Mark where platelets are.
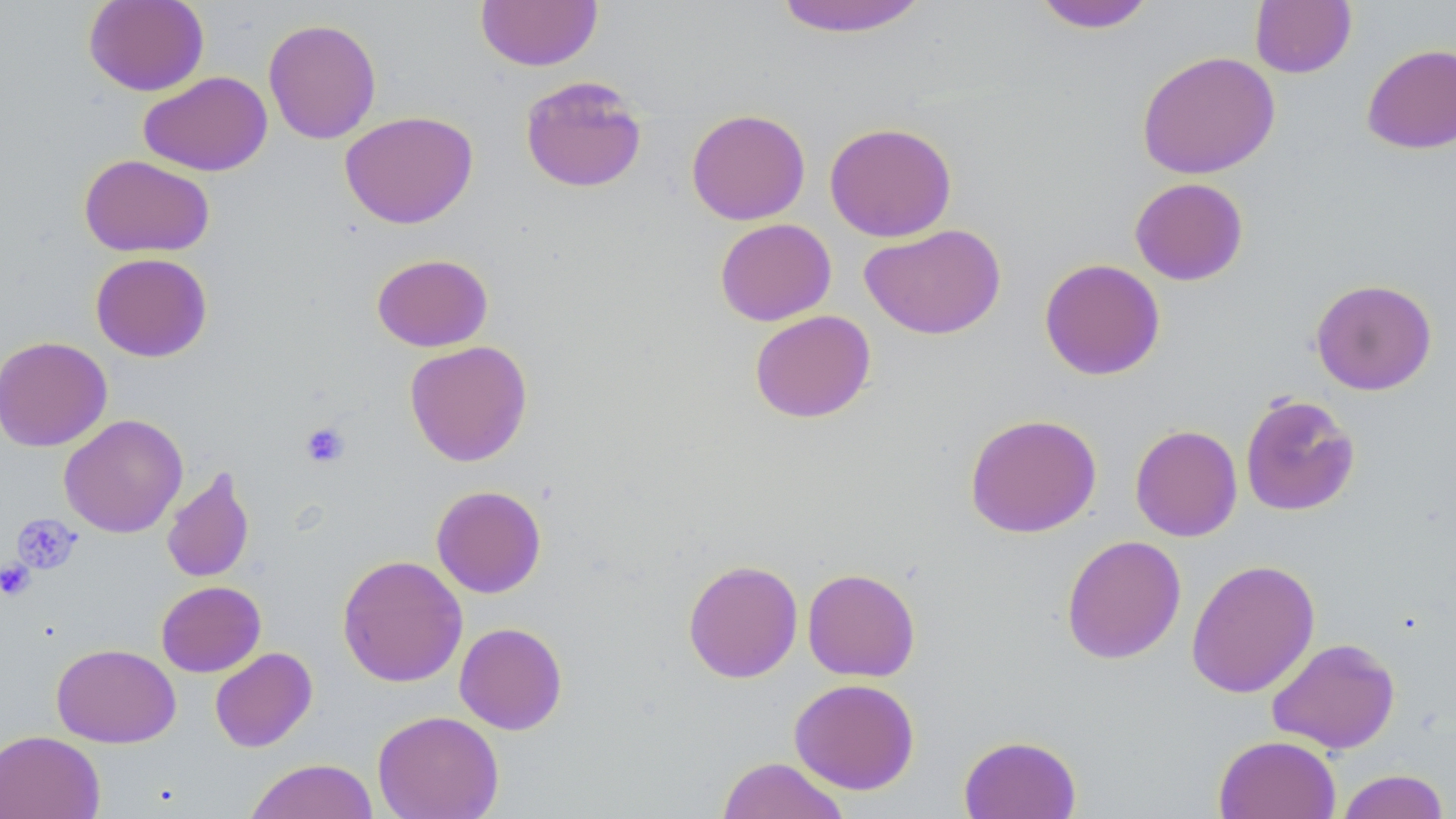

Approximate bounding boxes as [x1, y1, x2, y2] in pixels.
Platelets: [300, 421, 350, 468], [12, 514, 81, 573], [0, 559, 35, 600].

Uninfected red blood cell locations: [84, 0, 209, 96], [475, 0, 603, 71], [773, 0, 931, 37], [1032, 1, 1156, 33], [1250, 1, 1356, 78], [263, 18, 382, 144], [1361, 43, 1456, 154], [1137, 50, 1280, 179], [139, 71, 272, 176], [519, 75, 648, 193], [686, 109, 810, 225], [340, 110, 478, 229], [824, 121, 957, 242], [79, 154, 214, 257], [1129, 177, 1248, 285], [714, 218, 837, 326], [860, 223, 1006, 340], [90, 252, 213, 362], [371, 253, 493, 352], [1039, 258, 1165, 381], [1310, 278, 1437, 396], [749, 310, 876, 424], [0, 335, 112, 452], [404, 340, 533, 467], [1240, 393, 1360, 517], [964, 413, 1102, 538], [59, 414, 188, 538], [1130, 424, 1243, 542], [162, 466, 256, 584], [431, 485, 547, 598], [1061, 534, 1186, 664], [337, 554, 467, 688], [682, 559, 803, 683], [1186, 559, 1320, 698], [802, 567, 920, 681], [156, 580, 266, 677], [454, 622, 568, 735], [1266, 637, 1400, 754], [52, 643, 180, 747], [209, 647, 317, 753], [789, 678, 920, 794], [372, 710, 504, 819], [0, 729, 105, 819], [959, 734, 1082, 819], [1213, 734, 1341, 819], [716, 756, 851, 819], [244, 758, 379, 819], [1335, 769, 1450, 819]. Slide-level diagnosis: no evidence of blood parasites. Image is 1456×819 pixels. 1000x magnification. Thin blood film. May-Grünwald-Giemsa-stained preparation. Light microscopy. One field of a larger specimen.